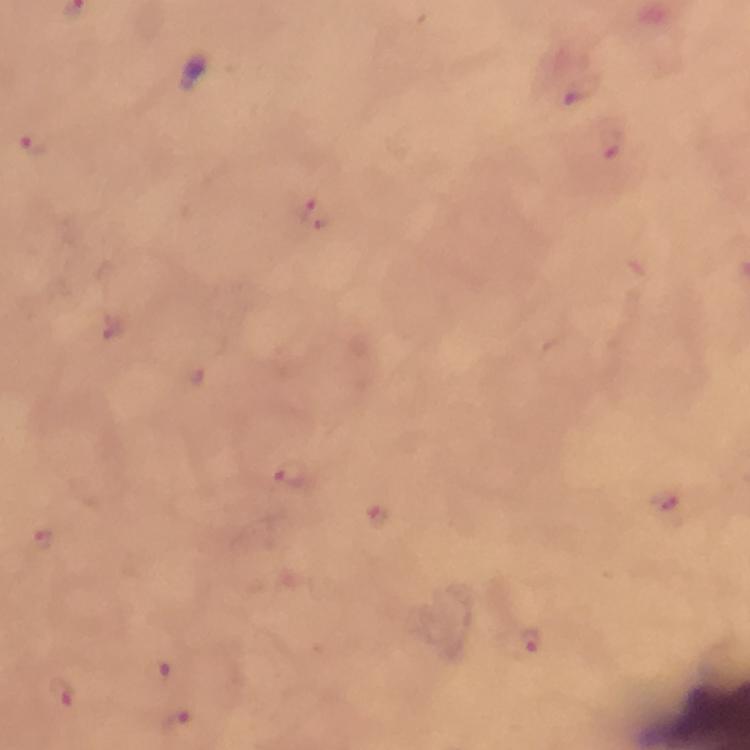
capture = smartphone photograph through a microscope
immersion oil = used
cropped from = a single field of view
stain = Giemsa
preparation = thick blood smear
image size = 750×750 pixels
Plasmodium parasite locations = approximate centers as (x, y) in pixels: (581, 90), (609, 142), (33, 144), (315, 211), (291, 475), (667, 504), (380, 515), (50, 547), (530, 641), (158, 670), (62, 693), (177, 720)
context = from a diagnostic examination for malaria
magnification = 100x